Assess this cell for malaria.
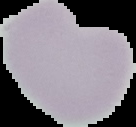
Uninfected.

image size = 136×127 pixels
preparation = thin blood smear
image type = segmented cell region with the area outside set to black